Locate every blood parasite and identify its species.
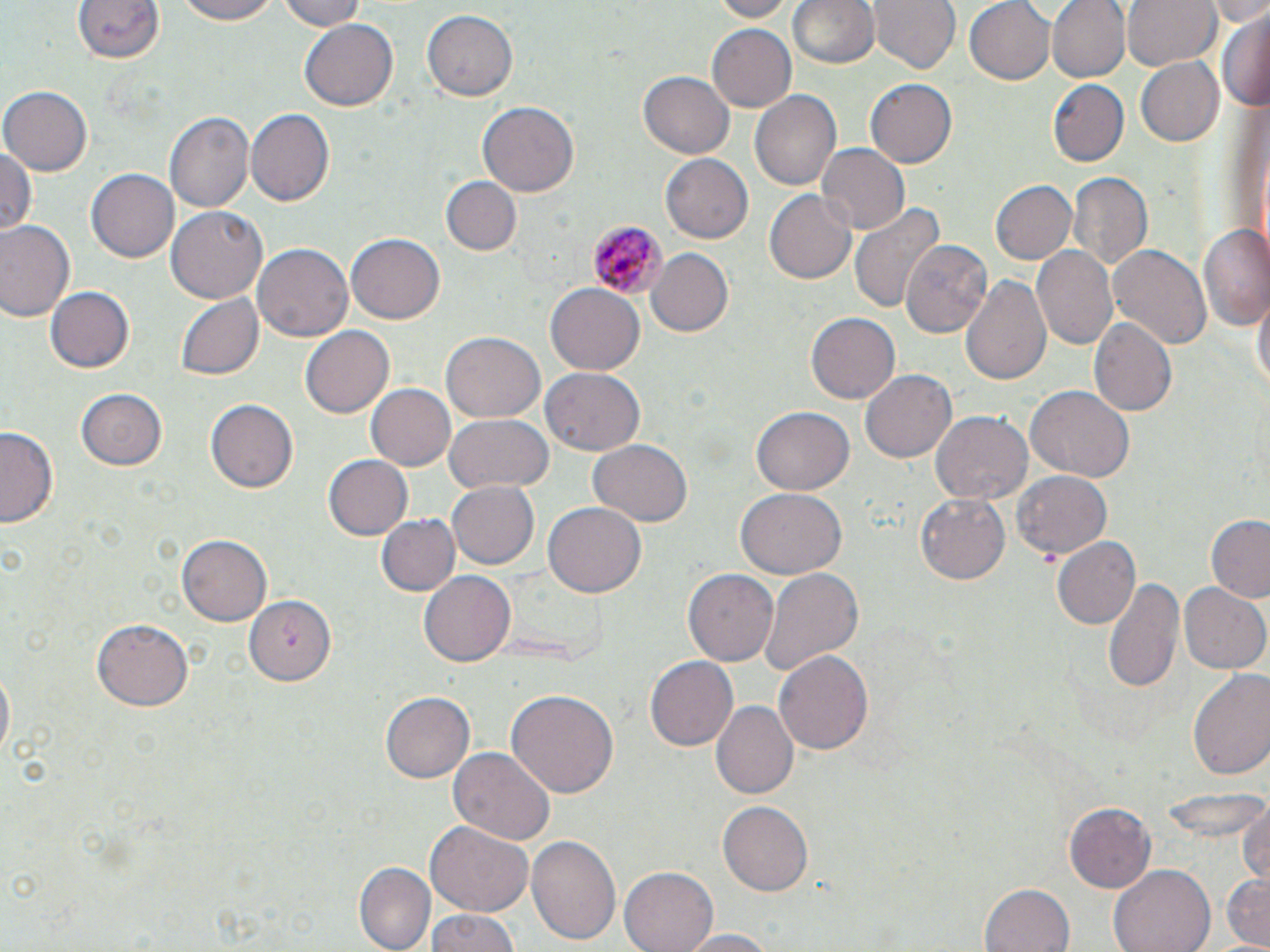

Approximate bounding boxes as (x1,y1)-(x2,y2) corner pairs in pixels.
Plasmodium malariae-infected red blood cells: (589,219)-(665,301).
No Plasmodium falciparum, Plasmodium ovale, Plasmodium vivax, Babesia divergens, or Trypanosoma brucei observed.

Summary:
  - Uninfected red blood cell locations: (171,0)-(288,25), (280,0)-(368,30), (703,0)-(800,21), (786,0)-(881,74), (867,0)-(959,76), (963,0)-(1055,84), (1046,0)-(1129,82), (1120,0)-(1221,72), (1205,0)-(1270,26), (70,2)-(167,72), (1217,10)-(1269,112), (420,11)-(516,101), (299,19)-(400,113), (707,24)-(797,113), (1135,57)-(1226,147), (640,70)-(735,158), (865,78)-(956,169), (1047,79)-(1128,167), (1,88)-(91,175), (751,88)-(841,191), (478,101)-(580,196), (246,108)-(334,206), (166,111)-(255,214), (1,141)-(37,240), (816,143)-(910,235), (659,154)-(753,245), (86,169)-(179,263), (1068,172)-(1152,273), (442,176)-(521,255), (991,179)-(1077,264), (765,192)-(856,282), (848,202)-(943,315), (165,204)-(267,304), (0,221)-(77,323), (1197,224)-(1270,330), (346,232)-(446,325), (900,237)-(993,336), (253,241)-(355,342), (1106,243)-(1212,353), (1031,246)-(1118,352), (645,249)-(735,338), (963,274)-(1051,387), (545,283)-(645,376), (44,285)-(134,374), (1252,291)-(1268,402), (177,295)-(264,379), (804,313)-(899,405), (1090,318)-(1177,417), (300,324)-(395,419), (441,333)-(546,422), (543,368)-(646,456), (862,368)-(957,463), (367,385)-(455,469), (1025,385)-(1135,482), (75,386)-(168,469), (207,399)-(298,493), (750,407)-(853,496), (930,412)-(1032,507), (444,416)-(552,494), (0,426)-(60,527), (587,440)-(693,528), (325,453)-(414,540), (1013,467)-(1114,560), (447,482)-(539,568), (736,488)-(846,579), (915,493)-(1008,585), (542,502)-(645,598), (376,512)-(460,595), (1205,516)-(1270,603), (178,534)-(276,624), (1053,538)-(1141,629), (684,568)-(780,666), (419,569)-(516,662), (759,569)-(862,678), (1100,574)-(1186,696), (1181,581)-(1270,674), (246,594)-(338,686), (92,619)-(195,711), (773,650)-(874,756), (643,655)-(739,753), (1,661)-(15,765), (1187,669)-(1270,784), (506,689)-(618,801), (382,691)-(476,784), (710,700)-(797,801), (449,747)-(554,844), (1237,798)-(1270,888), (719,801)-(813,897), (1064,801)-(1157,893), (425,823)-(533,917), (526,835)-(622,944), (353,863)-(430,952), (1111,863)-(1215,952), (619,865)-(720,952), (1219,870)-(1269,950), (980,884)-(1072,952), (422,909)-(521,952), (673,928)-(781,951)
  - Slide-level diagnosis: Plasmodium malariae
  - Magnification: 1000x
  - Modality: optical microscopy
  - Preparation: thin blood film
  - Stain: May-Grünwald-Giemsa
  - Image size: 1270×952 pixels
  - Field of view: one of a larger specimen